Locate and identify every blood parasite.
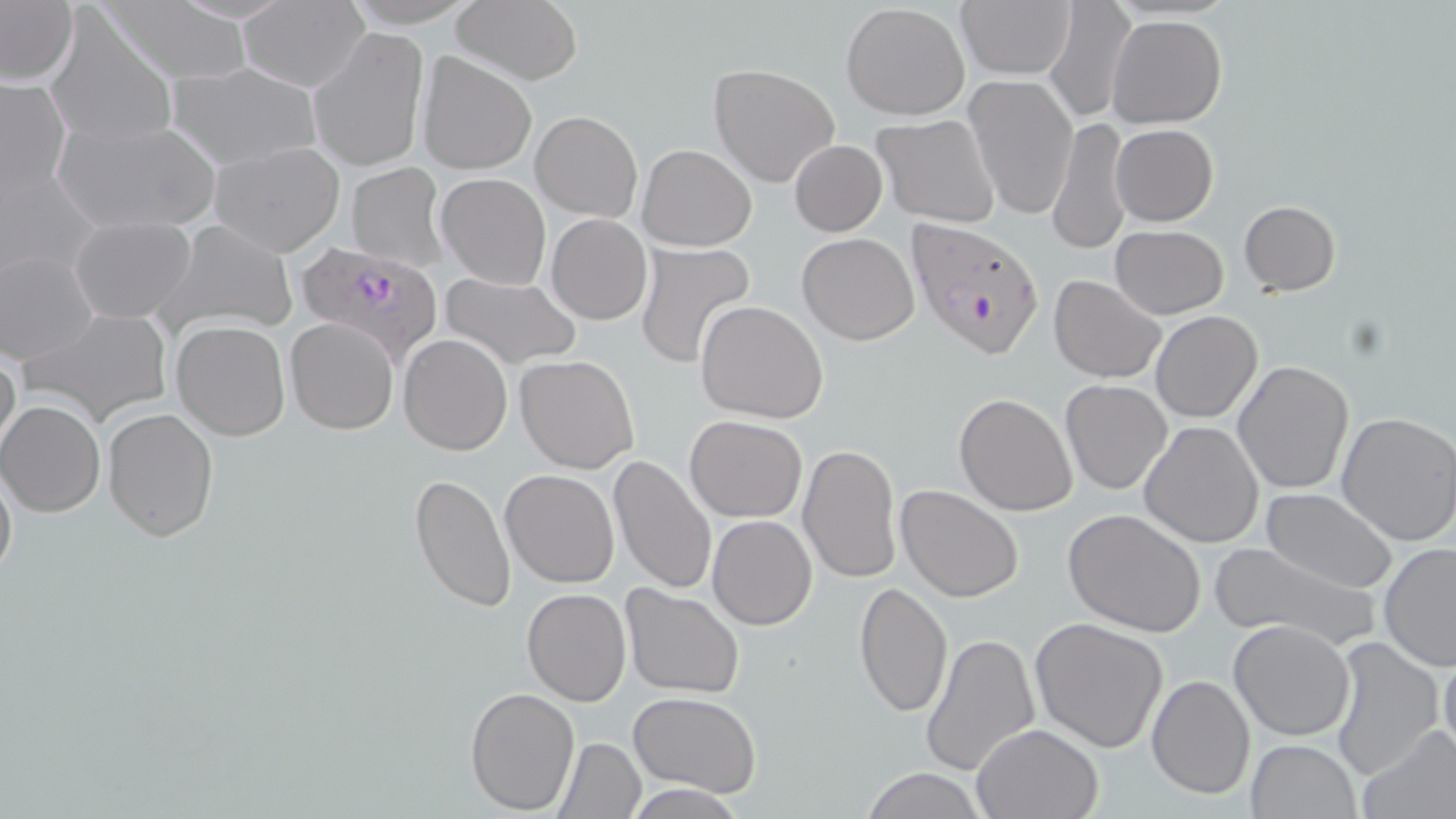
Approximate bounding boxes as (x1, y1, x2, y2) in pixels.
Plasmodium falciparum-infected red blood cells: (907, 217, 1045, 359), (294, 240, 446, 364).
No Plasmodium ovale, Plasmodium malariae, Plasmodium vivax, Babesia divergens, or Trypanosoma brucei observed.

Summary:
  - Uninfected red blood cell locations: (0, 0, 78, 89), (101, 0, 255, 88), (1045, 0, 1139, 126), (450, 1, 583, 84), (840, 2, 969, 121), (957, 2, 1075, 79), (238, 3, 369, 91), (46, 10, 177, 148), (1107, 14, 1227, 129), (309, 26, 429, 175), (418, 51, 535, 174), (167, 61, 321, 169), (707, 63, 840, 187), (964, 73, 1078, 220), (1, 77, 71, 201), (531, 110, 642, 223), (873, 115, 1000, 227), (1048, 115, 1133, 255), (53, 117, 220, 237), (1110, 123, 1218, 226), (210, 140, 347, 256), (790, 140, 887, 235), (637, 142, 757, 251), (346, 162, 449, 273), (0, 165, 100, 279), (437, 173, 550, 288), (1239, 200, 1341, 296), (546, 213, 652, 325), (69, 214, 198, 322), (154, 219, 298, 336), (1109, 225, 1229, 319), (798, 233, 920, 345), (633, 241, 759, 369), (1, 250, 100, 365), (442, 272, 580, 369), (1048, 275, 1165, 384), (695, 300, 829, 423), (24, 306, 172, 426), (1151, 311, 1262, 423), (285, 317, 399, 435), (171, 320, 290, 440), (398, 334, 514, 456), (0, 344, 21, 463), (515, 354, 640, 474), (1233, 360, 1354, 495), (1059, 379, 1172, 494), (953, 393, 1077, 516), (1, 400, 109, 517), (101, 407, 219, 543), (1335, 411, 1456, 546), (685, 415, 808, 522), (1139, 420, 1263, 547), (798, 442, 901, 585), (608, 456, 717, 596), (0, 460, 17, 585), (500, 469, 619, 587), (407, 472, 517, 614), (897, 485, 1023, 603), (1262, 489, 1396, 594), (1062, 508, 1208, 636), (707, 514, 817, 631), (1207, 540, 1377, 650), (1379, 541, 1456, 669), (854, 582, 953, 720), (620, 584, 745, 698), (521, 587, 631, 707), (1029, 619, 1170, 755), (1229, 620, 1355, 742), (921, 631, 1038, 778), (1329, 635, 1445, 783), (1438, 642, 1455, 767), (1147, 673, 1256, 800), (465, 687, 579, 812), (629, 690, 764, 798), (973, 723, 1103, 818), (1357, 723, 1456, 819), (554, 737, 646, 818), (1245, 739, 1360, 818), (856, 768, 988, 819), (627, 779, 748, 817)
  - Slide-level diagnosis: Plasmodium falciparum
  - Modality: light microscopy
  - Field of view: one of a larger specimen
  - Stain: May-Grünwald-Giemsa
  - Preparation: thin blood film
  - Image size: 1456×819 pixels
  - Magnification: 1000x